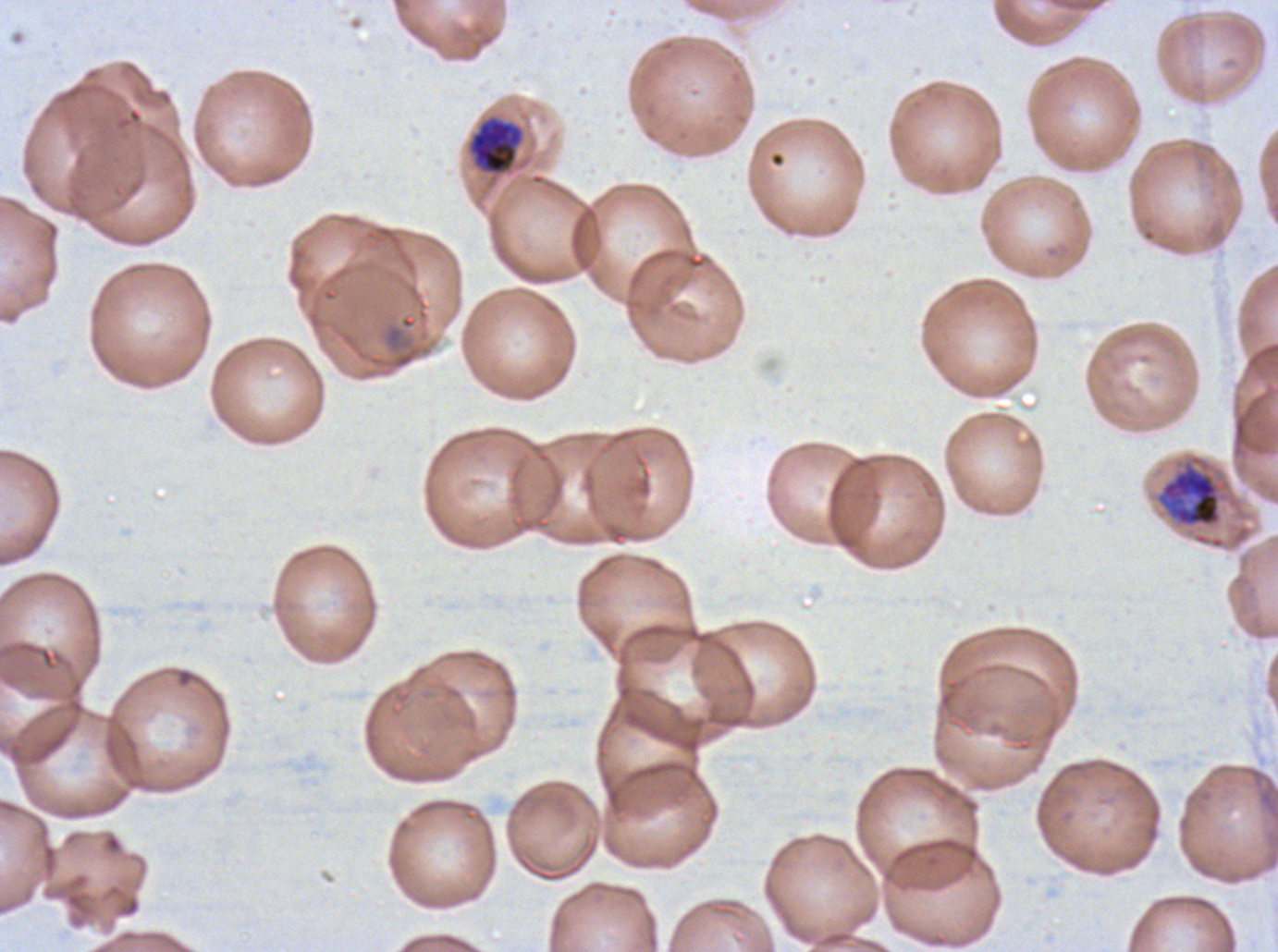
notation = approximate bounding boxes as {x1, y1, x2, y2} in pixels
mid trophozoite locations = {468, 116, 524, 176}
early schizont locations = {1157, 460, 1222, 527}
image size = 1278×952 pixels
field of view = sub-image separated from a larger composite
preparation = thin blood film
life-cycle stages observed = mid trophozoite, early schizont
specimen = P. falciparum cultured ex vivo for 24 to 48 hours, from a patient in The Gambia
stain = Giemsa